Comment on the morphology of the erythrocytes.
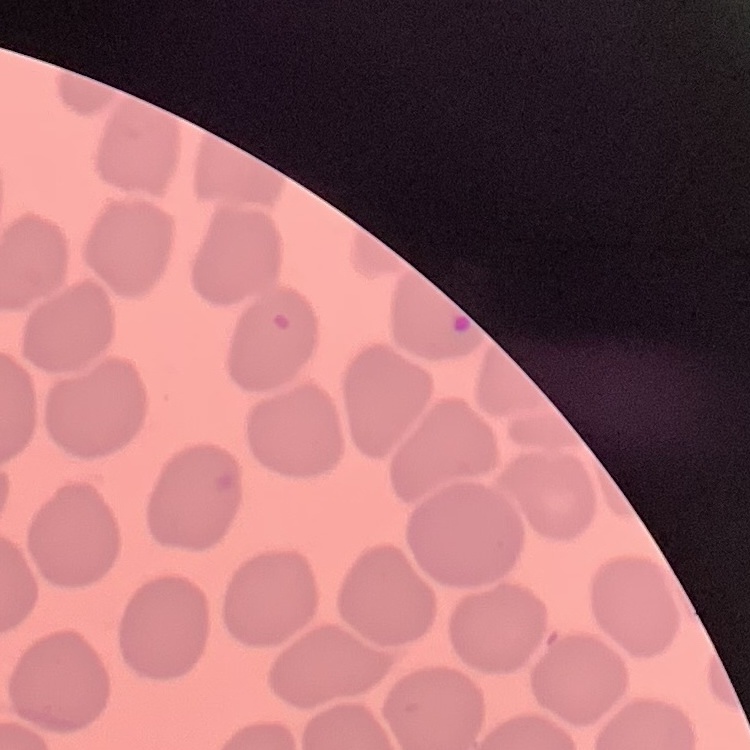

They show no rouleaux formation.

stain: Field's or Giemsa
preparation: thin blood smear
image_type: square crop of a larger photomicrograph